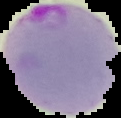

Summary:
  - Malaria status: parasitized
  - Image type: cell region segmented out of the field of view; surrounding area masked to black
  - Image size: 121×118 pixels
  - Preparation: thin blood film